Assess this cell for malaria.
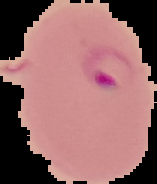
Parasitized.

preparation: thin blood smear
image_type: cell region segmented out of the field of view; surrounding area masked to black
image_size: 157×184 pixels